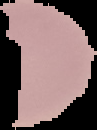
Summary:
  - Malaria status: uninfected
  - Preparation: thin blood film
  - Image size: 97×130 pixels
  - Image type: segmented cell region with the area outside set to black